Name the parasite shown.
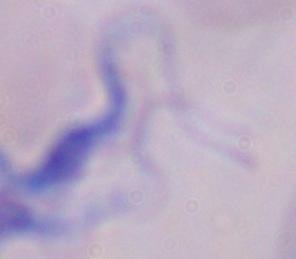

A trypanosome.

Summary:
  - Modality: photomicrograph
  - Magnification: 1000x